Comment on the morphology of the red blood cells.
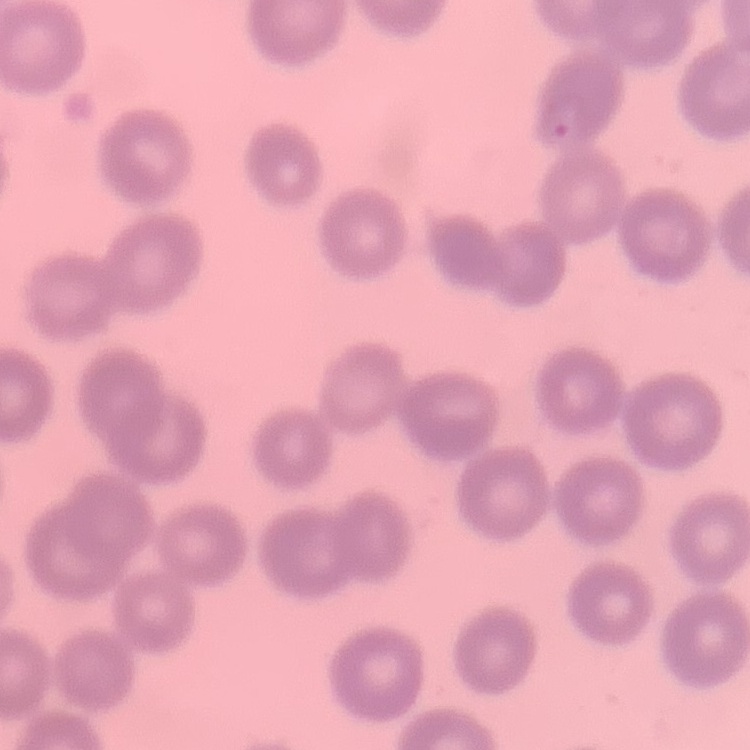
No rouleaux formation.

Summary:
  - Preparation: thin blood film
  - Stain: Field's or Giemsa
  - Image type: one tile cut from a larger photomicrograph